Look for parasitized red blood cells.
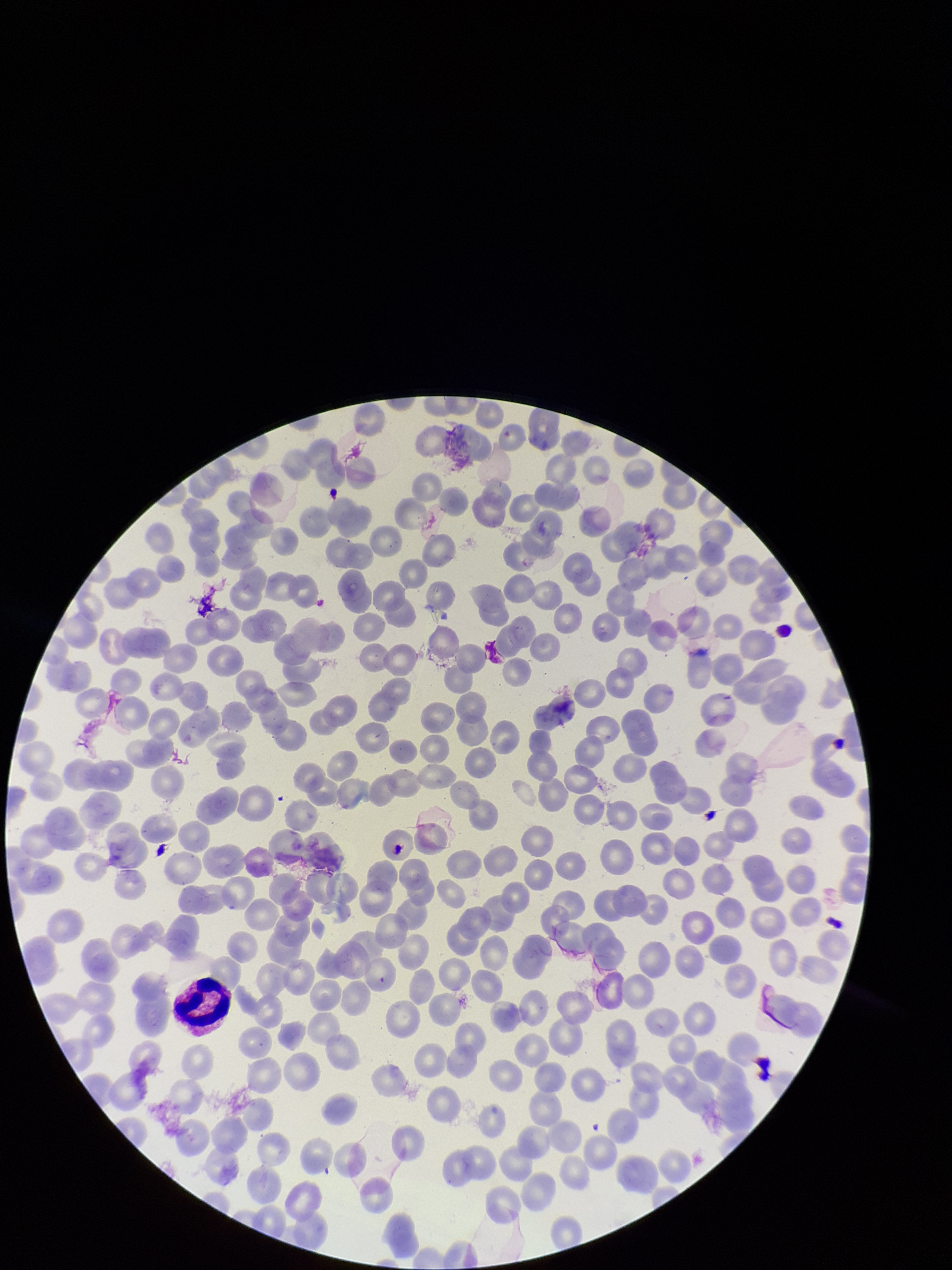
None identified.

Summary:
  - Capture: smartphone photograph through the microscope eyepiece
  - Field of view: one from this slide
  - Stain: Giemsa
  - Parasitized red blood cell count: 0
  - Red blood cell count: 229
  - Species reported for this patient: Plasmodium falciparum
  - Image size: 952×1270 pixels
  - Patient malaria status: infected
  - Preparation: thin